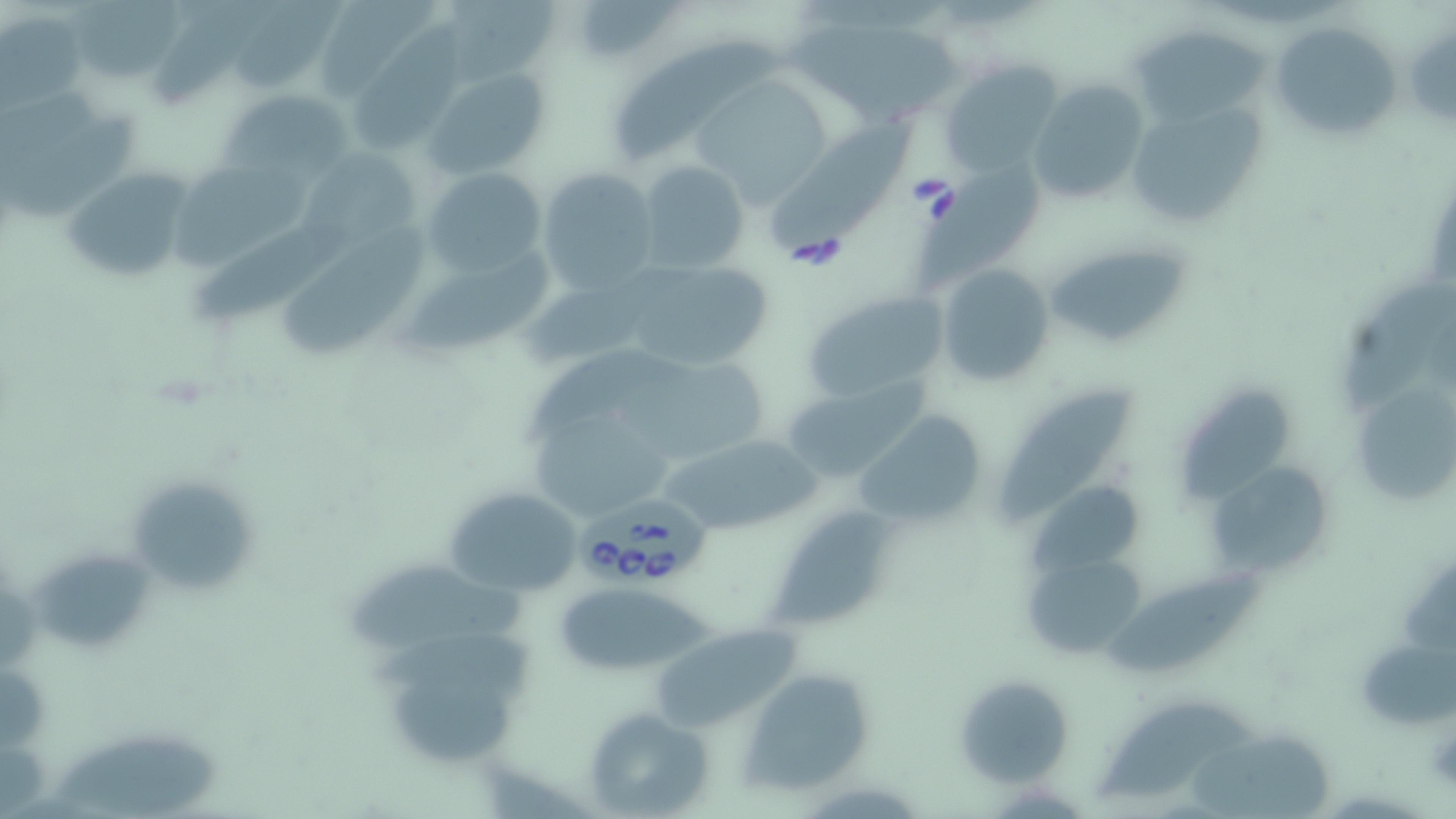

{
  "babesia_divergens_infected_red_blood_cell_locations": "approximate bounding boxes as (x1,y1)-(x2,y2) corner pairs in pixels: (580,490)-(715,590)",
  "slide_level_diagnosis": "Babesia divergens",
  "magnification": "1000x",
  "modality": "light microscopy",
  "field_of_view": "single",
  "stain": "May-Grünwald-Giemsa",
  "preparation": "thin blood film",
  "uninfected_red_blood_cell_locations": "approximate bounding boxes as (x1,y1)-(x2,y2) corner pairs in pixels: (68,0)-(181,82), (150,0)-(263,105), (316,0)-(445,100), (445,0)-(559,84), (574,0)-(681,60), (236,4)-(346,95), (2,10)-(86,108), (1269,19)-(1403,145), (346,24)-(479,154), (790,25)-(965,125), (1133,31)-(1268,121), (617,37)-(786,168), (941,61)-(1062,180), (427,67)-(551,179), (701,78)-(831,214), (1024,78)-(1149,207), (219,88)-(352,183), (1121,96)-(1267,230), (1,121)-(139,222), (774,126)-(913,260), (296,145)-(432,256), (636,160)-(752,275), (170,161)-(318,269), (60,165)-(196,285), (420,166)-(550,278), (538,167)-(659,295), (924,167)-(1040,284), (198,218)-(357,324), (279,229)-(434,357), (1047,236)-(1194,351), (406,253)-(558,353), (936,263)-(1054,385), (523,265)-(674,370), (633,268)-(774,371), (1345,281)-(1453,413), (799,289)-(955,403), (524,346)-(681,449), (607,357)-(771,465), (779,379)-(925,483), (1180,383)-(1294,504), (1003,389)-(1133,523), (1354,393)-(1452,504), (530,408)-(668,512), (853,410)-(991,529), (660,431)-(825,540), (1203,458)-(1336,582), (1024,481)-(1146,576), (131,484)-(256,591), (443,485)-(588,597), (771,513)-(883,626), (32,552)-(149,653), (347,559)-(530,641), (1030,568)-(1145,649), (1114,568)-(1267,677), (558,587)-(725,673), (646,626)-(814,732), (1358,628)-(1453,740), (366,630)-(536,708), (389,669)-(521,765), (738,670)-(879,794), (953,671)-(1073,784), (1098,694)-(1256,802), (581,707)-(714,818), (1190,729)-(1334,816), (47,733)-(225,819)",
  "image_size": "1456×819 pixels"
}